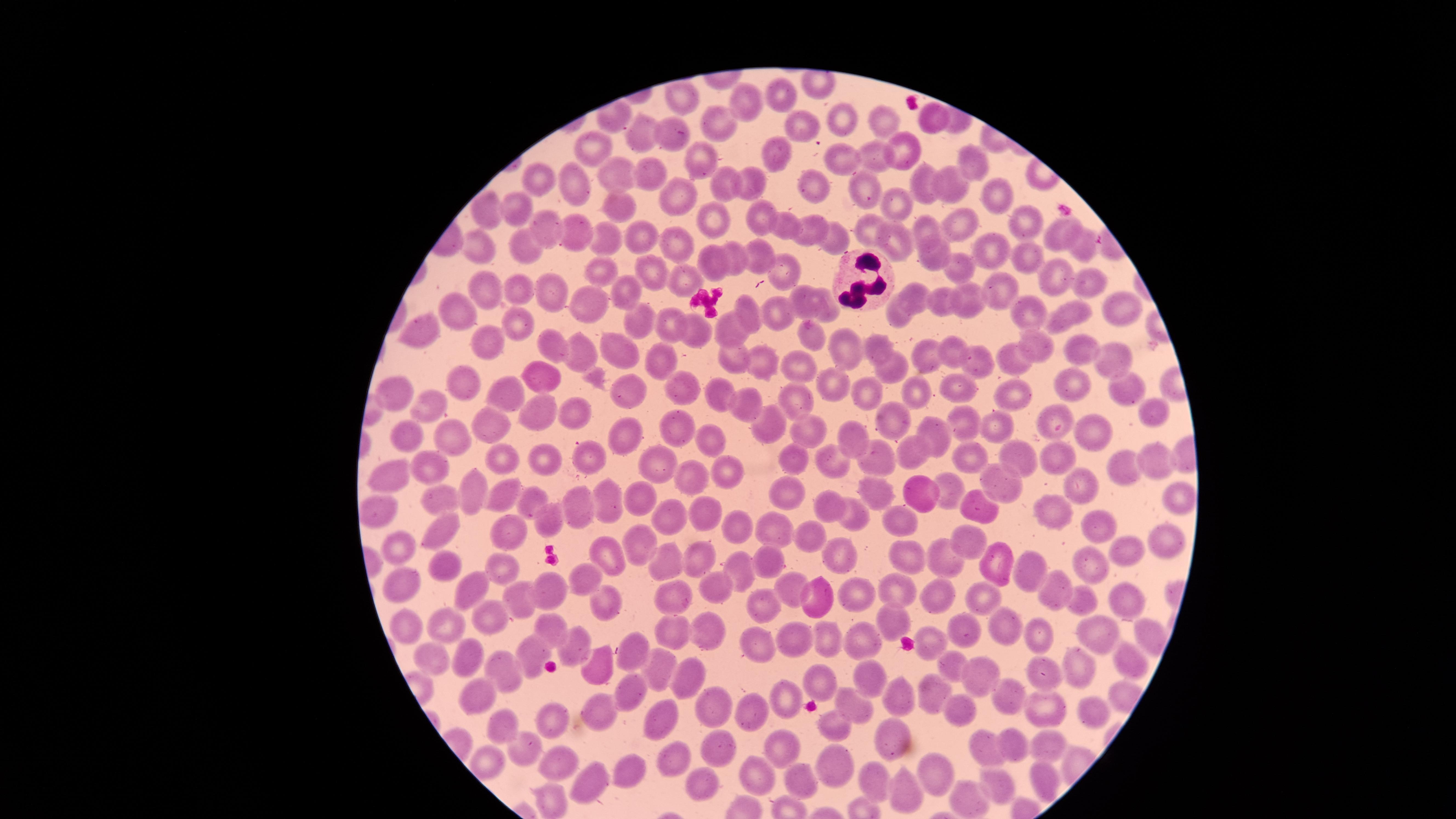
{
  "field_of_view": "single",
  "preparation": "thin blood film",
  "white_blood_cells": "approximate marker points, in pixels from the top-left corner: (x=861, y=280)",
  "visible_region": "circular",
  "image_size": "1456×819 pixels",
  "capture": "smartphone photograph through the microscope eyepiece",
  "presence": "no malaria parasites identified",
  "uninfected_red_blood_cells": "approximate marker points, in pixels from the top-left corner: (x=688, y=98), (x=790, y=101), (x=749, y=102), (x=838, y=118), (x=721, y=119), (x=932, y=119), (x=800, y=121), (x=883, y=124), (x=665, y=134), (x=640, y=140), (x=906, y=150), (x=776, y=151), (x=594, y=152), (x=844, y=153), (x=708, y=156), (x=873, y=159), (x=971, y=163), (x=648, y=174), (x=610, y=176), (x=536, y=181), (x=811, y=182), (x=954, y=182), (x=727, y=183), (x=750, y=183), (x=924, y=183), (x=572, y=187), (x=864, y=187), (x=993, y=193), (x=678, y=196), (x=621, y=202), (x=518, y=206), (x=899, y=207), (x=488, y=216), (x=716, y=217), (x=761, y=218), (x=1019, y=224), (x=546, y=225), (x=961, y=226), (x=789, y=227), (x=813, y=227), (x=871, y=230), (x=929, y=231), (x=1054, y=231), (x=580, y=234), (x=639, y=234), (x=833, y=234), (x=895, y=239), (x=607, y=240), (x=674, y=242), (x=527, y=244), (x=1083, y=245), (x=994, y=247), (x=478, y=248), (x=753, y=248), (x=1025, y=251), (x=925, y=256), (x=736, y=258), (x=709, y=262), (x=781, y=268), (x=649, y=271), (x=602, y=272), (x=963, y=272), (x=1049, y=277), (x=685, y=279), (x=484, y=283), (x=1083, y=287), (x=523, y=290), (x=548, y=290), (x=628, y=290), (x=1004, y=292), (x=916, y=297), (x=804, y=300), (x=944, y=304), (x=587, y=306), (x=970, y=306), (x=823, y=307), (x=1113, y=308), (x=1024, y=310), (x=748, y=312), (x=775, y=314), (x=1068, y=316), (x=461, y=317), (x=897, y=317), (x=514, y=320), (x=639, y=320), (x=421, y=327), (x=670, y=328), (x=696, y=333), (x=725, y=333), (x=810, y=337), (x=484, y=343), (x=620, y=343), (x=1038, y=343), (x=554, y=349), (x=851, y=350), (x=881, y=350), (x=1082, y=351), (x=953, y=355), (x=581, y=358), (x=928, y=358), (x=762, y=360), (x=656, y=361), (x=733, y=361), (x=1113, y=361), (x=1019, y=362), (x=891, y=364), (x=982, y=364), (x=794, y=365), (x=537, y=372), (x=460, y=381), (x=832, y=383), (x=868, y=387), (x=1070, y=388), (x=955, y=389), (x=631, y=390), (x=1124, y=390), (x=393, y=391), (x=683, y=391), (x=714, y=392), (x=1017, y=393), (x=505, y=394), (x=913, y=399), (x=798, y=400), (x=425, y=403), (x=751, y=403), (x=579, y=411), (x=1148, y=411), (x=535, y=412), (x=1058, y=413), (x=895, y=416), (x=491, y=419), (x=676, y=427), (x=807, y=428), (x=969, y=429), (x=767, y=430), (x=1001, y=430), (x=631, y=432), (x=935, y=432), (x=414, y=436), (x=1102, y=437), (x=713, y=439), (x=856, y=439), (x=457, y=442), (x=906, y=453), (x=792, y=455), (x=877, y=455), (x=1025, y=455), (x=1051, y=456), (x=591, y=457), (x=970, y=459), (x=512, y=460), (x=650, y=460), (x=1151, y=460), (x=550, y=461), (x=1126, y=463), (x=832, y=465), (x=444, y=466), (x=728, y=474), (x=379, y=477), (x=693, y=481), (x=1079, y=484), (x=996, y=486), (x=947, y=488), (x=469, y=490), (x=791, y=491), (x=920, y=491), (x=876, y=493), (x=1175, y=494), (x=607, y=496), (x=638, y=496), (x=503, y=497), (x=442, y=501), (x=831, y=503), (x=532, y=504), (x=975, y=506), (x=1047, y=508), (x=582, y=511), (x=706, y=513), (x=381, y=514), (x=854, y=515), (x=665, y=516), (x=548, y=518), (x=740, y=525), (x=906, y=527), (x=435, y=531), (x=777, y=531), (x=511, y=532), (x=1103, y=533), (x=813, y=537), (x=1170, y=540), (x=638, y=542), (x=971, y=542), (x=402, y=547), (x=604, y=551), (x=1136, y=551), (x=907, y=556), (x=998, y=556), (x=697, y=558), (x=841, y=558), (x=437, y=560), (x=501, y=561), (x=952, y=561), (x=666, y=563), (x=770, y=563), (x=738, y=565), (x=1092, y=565), (x=1025, y=570), (x=589, y=579), (x=401, y=582), (x=464, y=584), (x=717, y=585), (x=897, y=586), (x=790, y=587), (x=549, y=588), (x=676, y=588), (x=1047, y=589), (x=855, y=592), (x=517, y=597), (x=602, y=599), (x=763, y=599), (x=817, y=599), (x=933, y=599), (x=1121, y=600), (x=1085, y=602), (x=984, y=604), (x=896, y=617), (x=488, y=620), (x=544, y=621), (x=406, y=623), (x=449, y=627), (x=967, y=628), (x=716, y=630), (x=678, y=631), (x=1145, y=631), (x=1004, y=632), (x=795, y=637), (x=862, y=637), (x=820, y=638), (x=1035, y=638), (x=1099, y=638), (x=570, y=639), (x=930, y=641), (x=760, y=644), (x=628, y=649), (x=470, y=652), (x=541, y=653), (x=437, y=655), (x=1121, y=656), (x=596, y=662), (x=952, y=665), (x=656, y=666), (x=1087, y=669), (x=510, y=671), (x=975, y=672), (x=1044, y=675), (x=690, y=677), (x=816, y=681), (x=863, y=681), (x=626, y=685), (x=472, y=693), (x=929, y=694), (x=789, y=695), (x=903, y=695), (x=1007, y=695), (x=856, y=704), (x=710, y=706), (x=742, y=706), (x=1089, y=711), (x=597, y=712), (x=1044, y=712), (x=661, y=716), (x=561, y=724), (x=835, y=724), (x=497, y=725), (x=777, y=735), (x=889, y=737), (x=1020, y=742), (x=715, y=745), (x=1050, y=746), (x=991, y=747), (x=527, y=749), (x=675, y=755), (x=488, y=759), (x=832, y=763), (x=560, y=764), (x=631, y=771), (x=589, y=774), (x=756, y=774), (x=935, y=777), (x=873, y=781), (x=701, y=783), (x=804, y=784), (x=999, y=785), (x=1048, y=787), (x=902, y=794), (x=967, y=799), (x=552, y=803)",
  "stain": "Giemsa"
}